Classify this cell by malaria status.
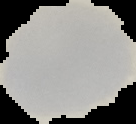

Uninfected.

Summary:
  - Image size: 136×124 pixels
  - Image type: segmented cell region with the area outside set to black
  - Preparation: thin blood film